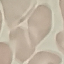

Summary:
  - Result: no malaria parasites detected
  - Stain: Giemsa
  - Image type: automatically extracted cell patch, resized to 64 × 64 pixels
  - Preparation: thin blood film
  - Capture: smartphone camera at the microscope eyepiece